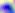

identification = Toxoplasma gondii
modality = micrograph
magnification = 400x